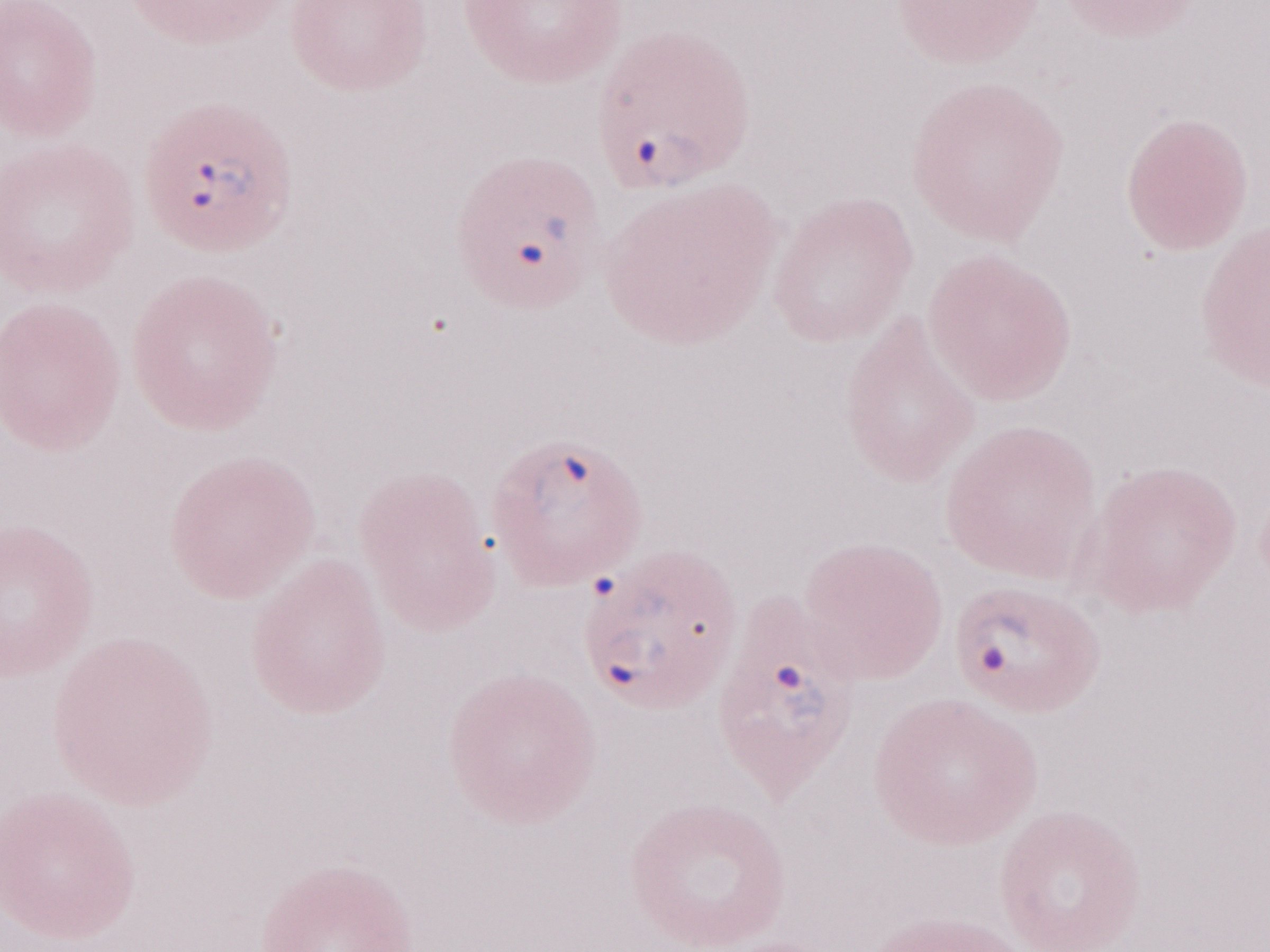

1,000x magnification. Olympus BX43 microscope and DP73 digital camera. May-Grünwald-Giemsa (MGG) stain. Thin blood smear. Patient-level malaria diagnosis: positive. Single field of view. Image is 1270×952 pixels.